Give the position of every malaria parasite and every leukocyte.
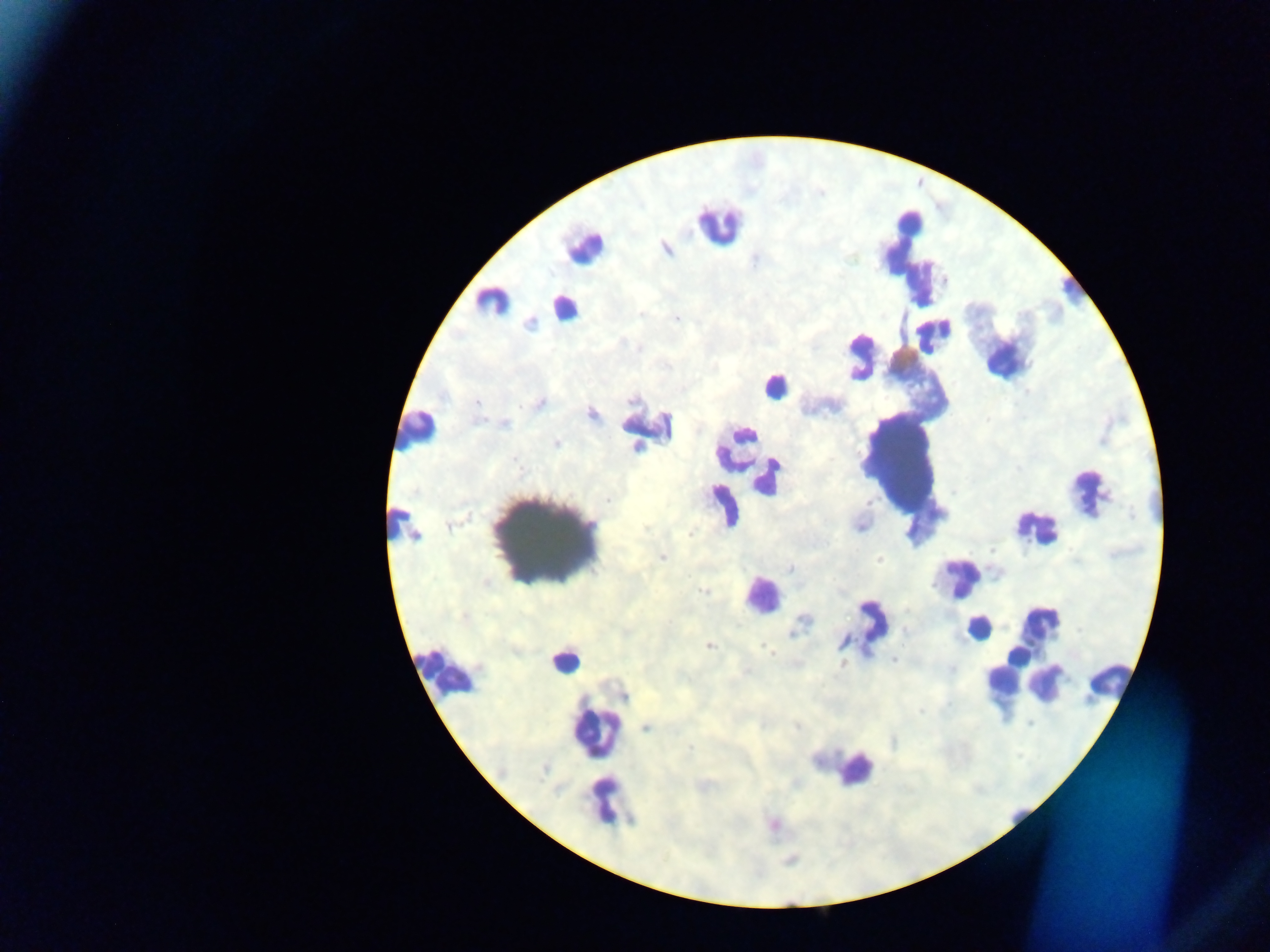
Approximate centers as {x, y} in pixels.
Malaria parasites: {664, 247}, {677, 319}, {530, 322}, {539, 402}, {591, 413}, {503, 423}, {557, 443}, {689, 534}, {663, 558}, {879, 560}, {788, 568}, {703, 590}, {708, 645}, {767, 649}, {772, 654}, {893, 660}, {843, 664}, {624, 695}, {921, 711}, {1028, 724}, {796, 726}, {647, 727}, {774, 824}, {790, 860}.
Leukocytes: {908, 222}, {719, 225}, {906, 237}, {583, 247}, {918, 278}, {1074, 288}, {493, 301}, {565, 307}, {933, 335}, {861, 354}, {1007, 357}, {773, 385}, {648, 425}, {418, 431}, {745, 434}, {739, 441}, {898, 454}, {767, 477}, {1089, 492}, {722, 504}, {404, 524}, {1036, 527}, {546, 541}, {959, 578}, {762, 596}, {1039, 622}, {868, 626}, {979, 627}, {1017, 657}, {565, 660}, {447, 672}, {1004, 682}, {1108, 682}, {1044, 684}, {595, 733}, {855, 768}, {605, 799}, {1017, 816}.

Summary:
  - Capture: mobile-phone photograph through a microscope
  - Preparation: thick blood film
  - Country: Ghana
  - Field of view: single
  - Image size: 1270×952 pixels